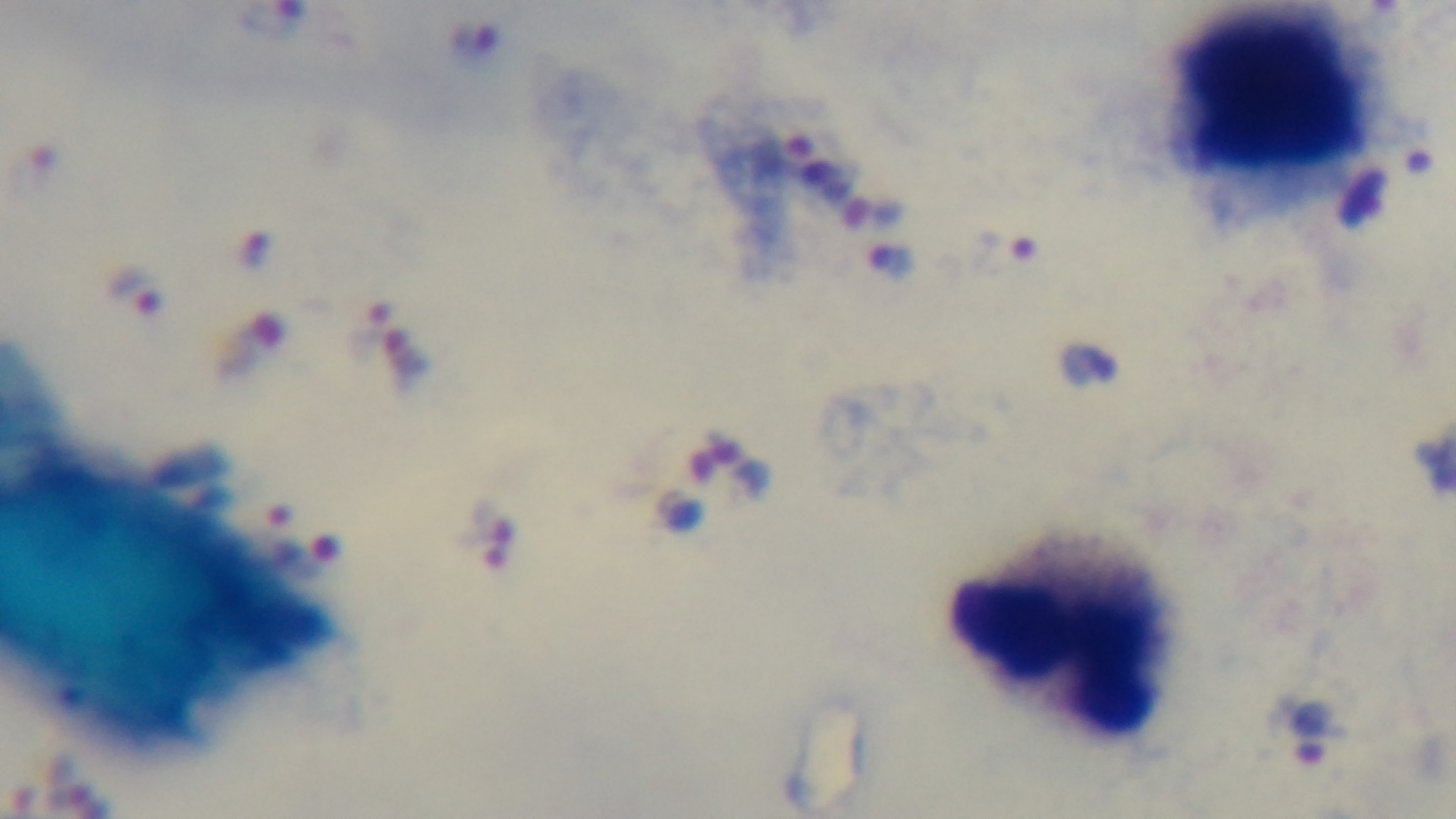

malaria status = positive
objective = 100x oil immersion
modality = light microscopy
capture = mounted 4K digital camera
stain = Giemsa
field of view = one from the slide
preparation = thick blood film